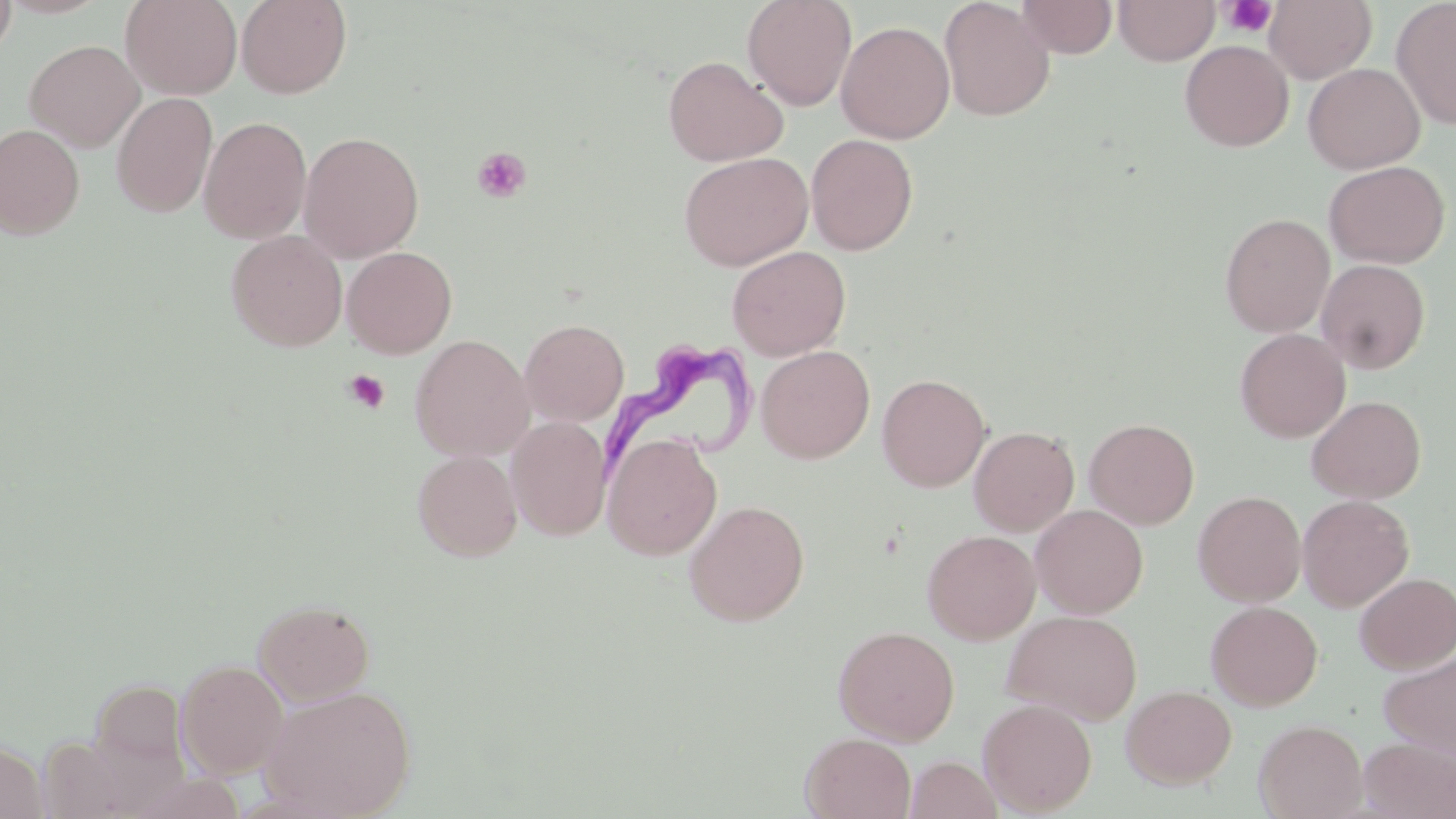
Approximate bounding boxes as named x1/y1/x2/y2 corners in pixels. Platelet locations: (x1=1220, y1=0, x2=1276, y2=38), (x1=472, y1=146, x2=531, y2=203), (x1=343, y1=369, x2=390, y2=414). Uninfected red blood cell locations: (x1=0, y1=0, x2=111, y2=19), (x1=0, y1=0, x2=17, y2=61), (x1=120, y1=0, x2=242, y2=100), (x1=236, y1=0, x2=352, y2=99), (x1=742, y1=0, x2=857, y2=111), (x1=938, y1=0, x2=1055, y2=122), (x1=1015, y1=0, x2=1117, y2=59), (x1=1113, y1=0, x2=1220, y2=65), (x1=1264, y1=0, x2=1377, y2=84), (x1=1392, y1=0, x2=1456, y2=129), (x1=836, y1=21, x2=955, y2=144), (x1=24, y1=39, x2=144, y2=152), (x1=1179, y1=39, x2=1294, y2=152), (x1=663, y1=55, x2=788, y2=167), (x1=1303, y1=62, x2=1425, y2=174), (x1=112, y1=92, x2=218, y2=218), (x1=198, y1=116, x2=312, y2=244), (x1=0, y1=124, x2=85, y2=240), (x1=299, y1=131, x2=424, y2=263), (x1=806, y1=133, x2=918, y2=255), (x1=678, y1=152, x2=813, y2=271), (x1=1323, y1=160, x2=1450, y2=268), (x1=1220, y1=213, x2=1335, y2=337), (x1=226, y1=230, x2=348, y2=352), (x1=727, y1=245, x2=851, y2=361), (x1=342, y1=247, x2=457, y2=358), (x1=1316, y1=259, x2=1430, y2=374), (x1=520, y1=318, x2=629, y2=426), (x1=1234, y1=328, x2=1350, y2=442), (x1=410, y1=335, x2=535, y2=462), (x1=755, y1=345, x2=875, y2=463), (x1=877, y1=373, x2=991, y2=492), (x1=1306, y1=395, x2=1427, y2=504), (x1=506, y1=415, x2=612, y2=540), (x1=1084, y1=418, x2=1199, y2=530), (x1=969, y1=426, x2=1079, y2=536), (x1=603, y1=433, x2=722, y2=560), (x1=412, y1=450, x2=522, y2=561), (x1=1193, y1=490, x2=1306, y2=607), (x1=1297, y1=494, x2=1414, y2=612), (x1=684, y1=499, x2=810, y2=626), (x1=1030, y1=505, x2=1148, y2=618), (x1=922, y1=529, x2=1041, y2=645), (x1=1354, y1=572, x2=1456, y2=673), (x1=252, y1=599, x2=376, y2=706), (x1=1205, y1=600, x2=1323, y2=710), (x1=1002, y1=610, x2=1142, y2=725), (x1=832, y1=625, x2=960, y2=745), (x1=1379, y1=650, x2=1456, y2=758), (x1=175, y1=659, x2=289, y2=779), (x1=87, y1=678, x2=191, y2=782), (x1=1120, y1=684, x2=1237, y2=789), (x1=258, y1=685, x2=416, y2=819), (x1=977, y1=698, x2=1097, y2=815), (x1=1254, y1=719, x2=1368, y2=819), (x1=800, y1=733, x2=916, y2=819), (x1=1358, y1=737, x2=1456, y2=819), (x1=0, y1=739, x2=49, y2=819), (x1=908, y1=739, x2=1062, y2=819), (x1=906, y1=756, x2=1001, y2=819). Trypanosoma brucei locations: (x1=597, y1=338, x2=761, y2=481). Slide-level diagnosis: Trypanosoma brucei. May-Grünwald-Giemsa-stained preparation. Single field of view. Thin blood smear. Captured at 1000x magnification. Light microscopy. Image is 1456×819 pixels.